Comment on the morphology of the red blood cells.
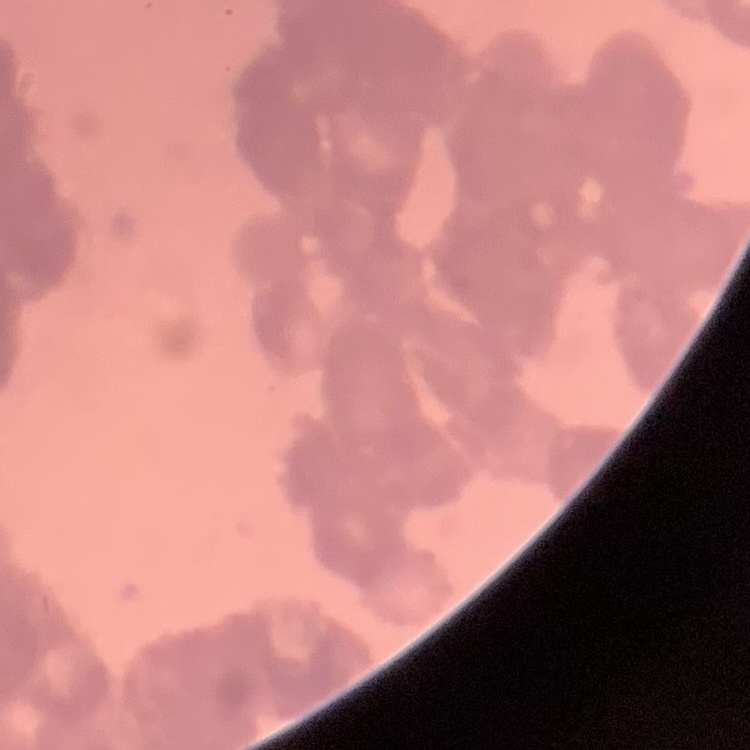
Rouleaux formation.

{
  "image_type": "square crop of a larger photomicrograph",
  "stain": "Field's or Giemsa",
  "preparation": "thin blood smear"
}